Name the parasite shown.
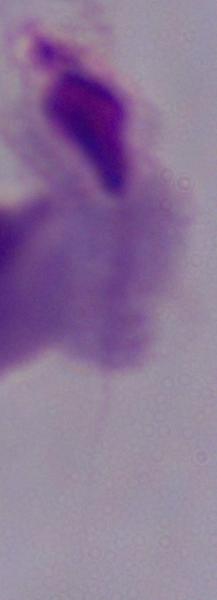

A trichomonad.

Micrograph. 1000x magnification.